Locate and identify every blood parasite.
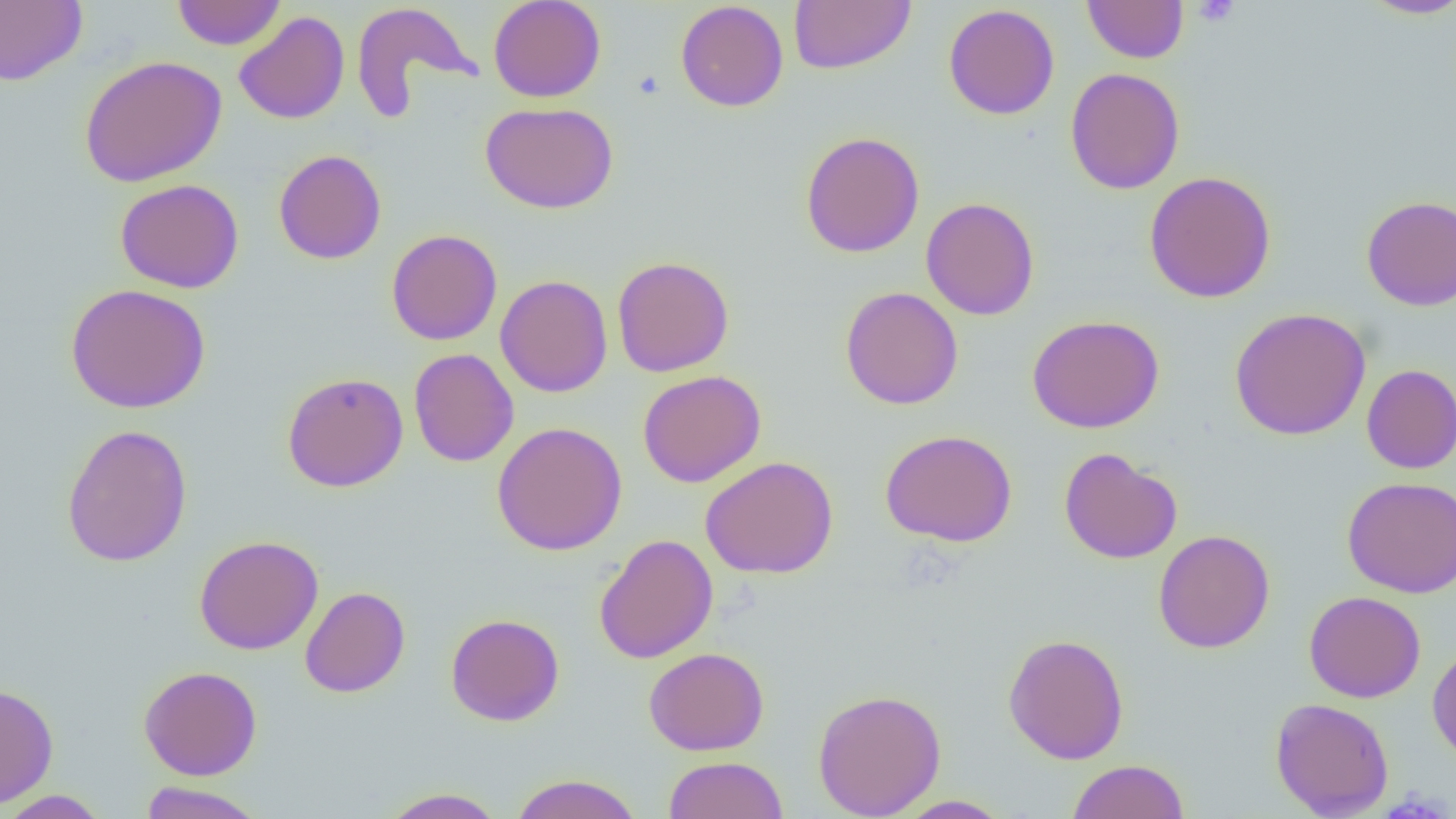

No blood parasites seen.

Summary:
  - Coordinate format: approximate bounding boxes as named x1/y1/x2/y2 corners in pixels
  - Uninfected red blood cell locations: (x1=171, y1=0, x2=287, y2=50), (x1=488, y1=0, x2=606, y2=103), (x1=1082, y1=0, x2=1188, y2=63), (x1=1358, y1=0, x2=1456, y2=19), (x1=0, y1=1, x2=87, y2=85), (x1=675, y1=1, x2=789, y2=112), (x1=789, y1=1, x2=916, y2=75), (x1=350, y1=2, x2=478, y2=119), (x1=943, y1=3, x2=1059, y2=120), (x1=234, y1=11, x2=350, y2=125), (x1=79, y1=55, x2=227, y2=188), (x1=1065, y1=67, x2=1185, y2=195), (x1=480, y1=101, x2=619, y2=214), (x1=800, y1=131, x2=925, y2=257), (x1=273, y1=149, x2=386, y2=265), (x1=1143, y1=171, x2=1277, y2=303), (x1=115, y1=178, x2=244, y2=294), (x1=1361, y1=195, x2=1456, y2=311), (x1=921, y1=197, x2=1039, y2=320), (x1=386, y1=229, x2=502, y2=346), (x1=611, y1=256, x2=734, y2=377), (x1=495, y1=274, x2=613, y2=398), (x1=65, y1=283, x2=211, y2=413), (x1=840, y1=286, x2=963, y2=410), (x1=1229, y1=307, x2=1371, y2=440), (x1=1027, y1=315, x2=1164, y2=434), (x1=408, y1=348, x2=519, y2=467), (x1=1361, y1=364, x2=1456, y2=474), (x1=638, y1=370, x2=766, y2=487), (x1=282, y1=372, x2=408, y2=492), (x1=492, y1=421, x2=628, y2=556), (x1=61, y1=423, x2=193, y2=567), (x1=880, y1=429, x2=1018, y2=547), (x1=1058, y1=447, x2=1182, y2=564), (x1=700, y1=456, x2=838, y2=579), (x1=1342, y1=476, x2=1456, y2=598), (x1=1153, y1=529, x2=1275, y2=654), (x1=594, y1=533, x2=719, y2=664), (x1=194, y1=535, x2=324, y2=655), (x1=300, y1=586, x2=410, y2=698), (x1=1304, y1=590, x2=1427, y2=703), (x1=446, y1=613, x2=564, y2=726), (x1=1002, y1=633, x2=1130, y2=764), (x1=1427, y1=643, x2=1456, y2=764), (x1=643, y1=647, x2=769, y2=755), (x1=139, y1=665, x2=263, y2=780), (x1=1, y1=682, x2=59, y2=808), (x1=812, y1=688, x2=947, y2=818), (x1=1269, y1=697, x2=1394, y2=818), (x1=664, y1=756, x2=788, y2=819), (x1=1067, y1=759, x2=1190, y2=819), (x1=508, y1=773, x2=644, y2=819), (x1=139, y1=781, x2=267, y2=819), (x1=379, y1=787, x2=506, y2=818), (x1=0, y1=789, x2=111, y2=818), (x1=892, y1=795, x2=1013, y2=818)
  - Platelet locations: (x1=1192, y1=0, x2=1241, y2=27), (x1=632, y1=71, x2=664, y2=100)
  - Slide-level diagnosis: negative for blood parasites
  - Field of view: single
  - Modality: light microscopy
  - Magnification: 1000x
  - Image size: 1456×819 pixels
  - Preparation: thin blood film